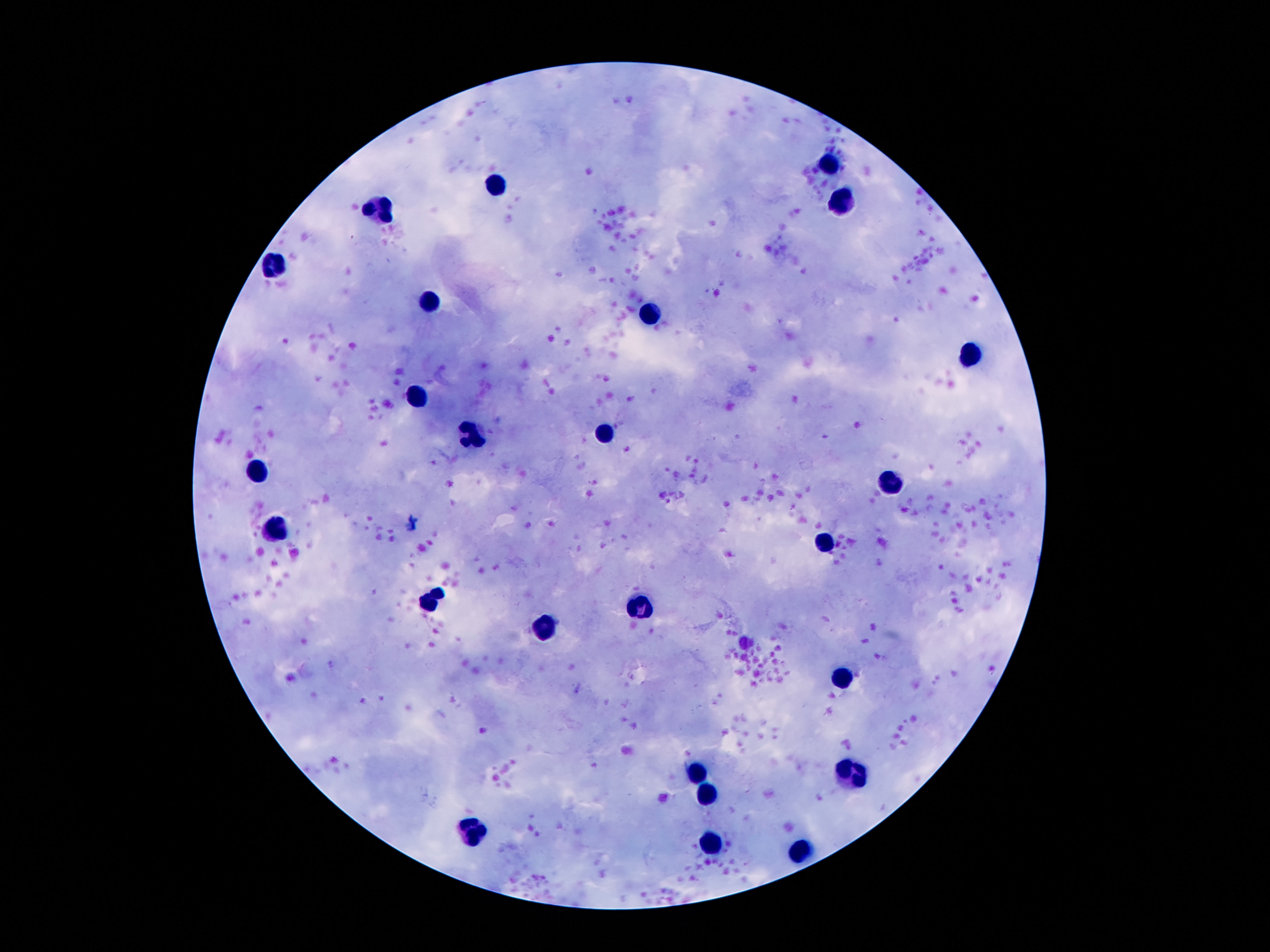

Approximate centers as (x, y) in pixels.
Summary:
  - Leukocyte locations: (834, 162), (496, 186), (841, 198), (378, 207), (277, 265), (429, 302), (649, 314), (971, 352), (417, 399), (470, 436), (606, 436), (258, 468), (892, 483), (277, 531), (827, 541), (429, 604), (640, 606), (544, 630), (841, 679), (697, 771), (853, 771), (705, 793), (474, 831), (709, 847), (801, 849)
  - Preparation: thick peripheral-blood smear
  - Patient malaria status: not infected
  - Capture: smartphone camera through the microscope eyepiece
  - Stain: Giemsa
  - Magnification: 100x
  - Field of view: single
  - Image size: 1270×952 pixels